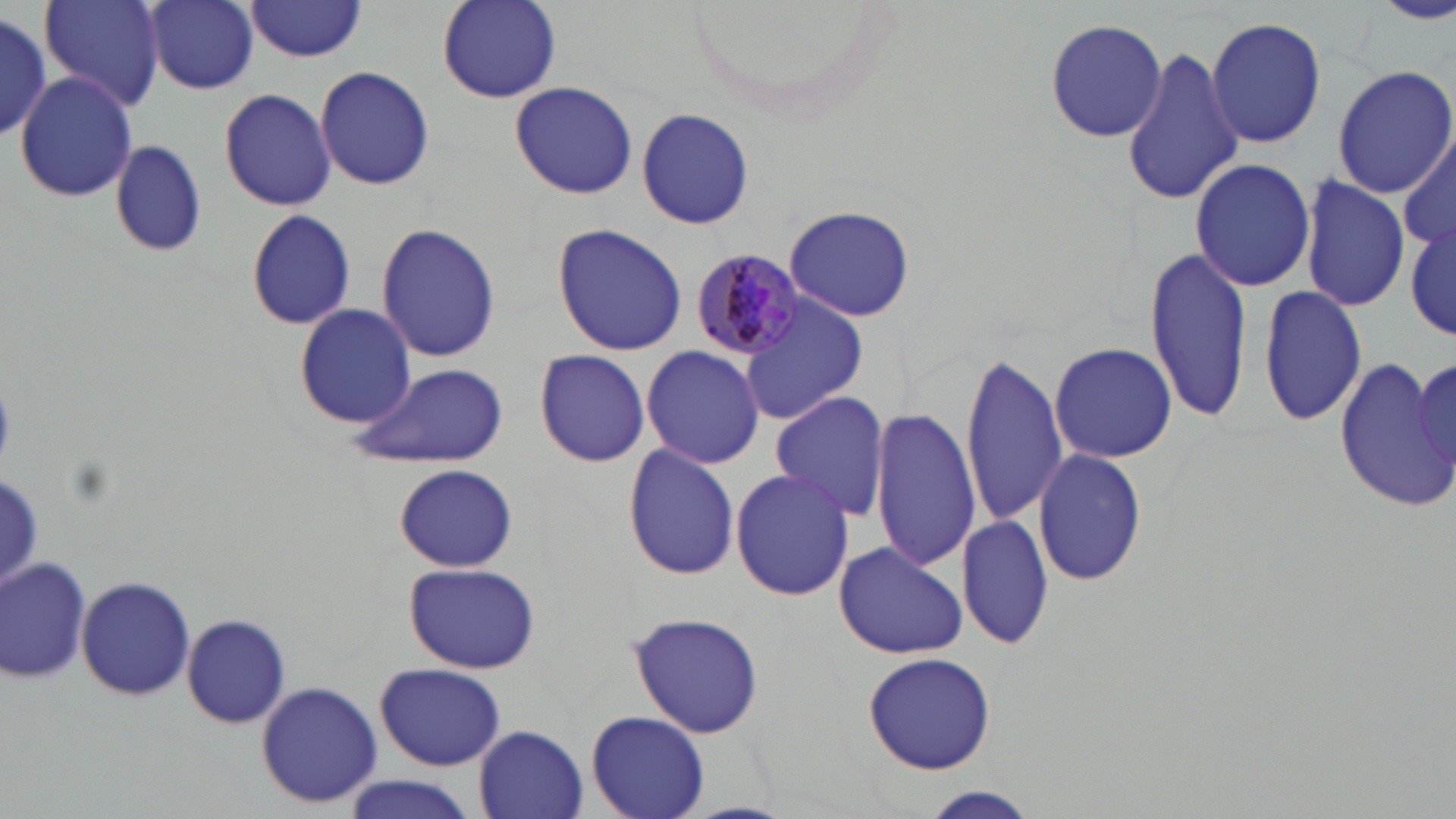

Summary:
  - Coordinate format: approximate bounding boxes as named x1/y1/x2/y2 corners in pixels
  - White blood cell locations: (x1=3, y1=553, x2=91, y2=685)
  - Uninfected red blood cell locations: (x1=42, y1=0, x2=164, y2=113), (x1=144, y1=0, x2=260, y2=93), (x1=438, y1=0, x2=562, y2=103), (x1=1377, y1=0, x2=1456, y2=24), (x1=243, y1=1, x2=369, y2=61), (x1=0, y1=14, x2=51, y2=140), (x1=1206, y1=16, x2=1326, y2=148), (x1=1044, y1=18, x2=1168, y2=141), (x1=1122, y1=42, x2=1243, y2=209), (x1=1332, y1=64, x2=1455, y2=199), (x1=313, y1=65, x2=436, y2=191), (x1=16, y1=70, x2=139, y2=203), (x1=511, y1=80, x2=636, y2=199), (x1=219, y1=86, x2=336, y2=211), (x1=637, y1=106, x2=754, y2=230), (x1=109, y1=140, x2=206, y2=257), (x1=1400, y1=140, x2=1455, y2=252), (x1=1189, y1=159, x2=1317, y2=291), (x1=1298, y1=175, x2=1411, y2=312), (x1=781, y1=205, x2=915, y2=321), (x1=245, y1=209, x2=355, y2=330), (x1=1406, y1=216, x2=1454, y2=347), (x1=375, y1=224, x2=502, y2=364), (x1=554, y1=225, x2=688, y2=356), (x1=1145, y1=246, x2=1255, y2=426), (x1=1260, y1=283, x2=1369, y2=427), (x1=737, y1=294, x2=868, y2=425), (x1=294, y1=302, x2=416, y2=429), (x1=1050, y1=341, x2=1176, y2=463), (x1=641, y1=345, x2=767, y2=468), (x1=533, y1=349, x2=651, y2=467), (x1=1413, y1=353, x2=1456, y2=490), (x1=959, y1=354, x2=1069, y2=525), (x1=1331, y1=355, x2=1456, y2=513), (x1=346, y1=361, x2=509, y2=468), (x1=770, y1=390, x2=889, y2=522), (x1=871, y1=407, x2=978, y2=568), (x1=623, y1=444, x2=739, y2=580), (x1=1032, y1=448, x2=1150, y2=585), (x1=394, y1=465, x2=516, y2=572), (x1=732, y1=466, x2=853, y2=601), (x1=957, y1=513, x2=1054, y2=649), (x1=833, y1=540, x2=969, y2=660), (x1=2, y1=555, x2=91, y2=681), (x1=404, y1=561, x2=540, y2=675), (x1=76, y1=574, x2=195, y2=704), (x1=628, y1=610, x2=766, y2=740), (x1=183, y1=612, x2=291, y2=730), (x1=863, y1=651, x2=996, y2=775), (x1=374, y1=662, x2=507, y2=771), (x1=256, y1=681, x2=381, y2=807), (x1=586, y1=708, x2=708, y2=819), (x1=475, y1=726, x2=590, y2=818), (x1=343, y1=775, x2=480, y2=819), (x1=919, y1=787, x2=1040, y2=819)
  - Plasmodium malariae-infected red blood cell locations: (x1=690, y1=251, x2=807, y2=363)
  - Slide-level diagnosis: Plasmodium malariae
  - Image size: 1456×819 pixels
  - Magnification: 1000x
  - Stain: May-Grünwald-Giemsa
  - Field of view: single
  - Modality: optical microscopy
  - Preparation: thin blood smear